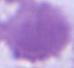

magnification = 1000x
identification = red blood cell
modality = photomicrograph